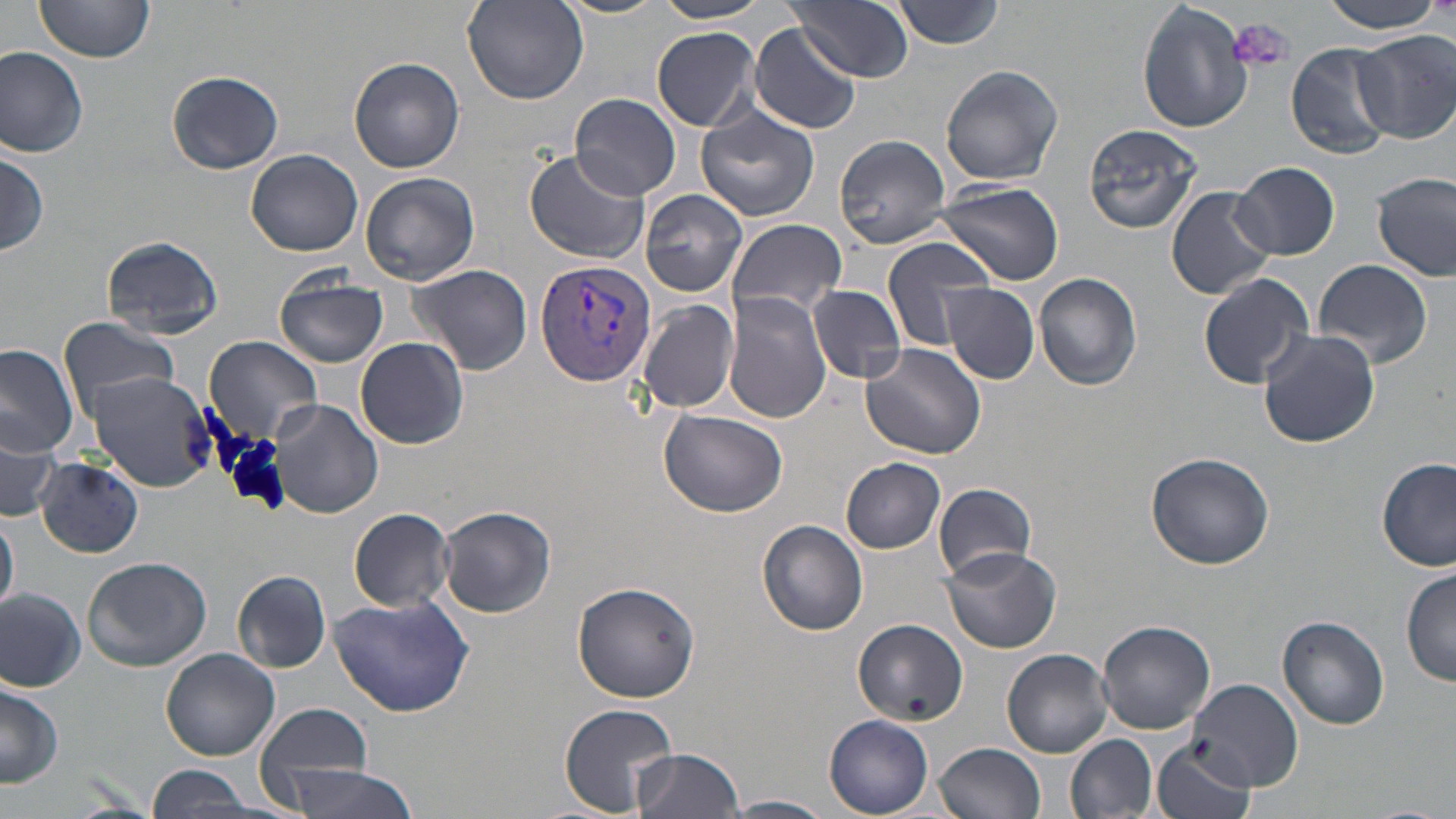 Approximate bounding boxes as (x1,y1)-(x2,y2) corner pairs in pixels. Platelet locations: (1227,18)-(1297,73). Uninfected red blood cell locations: (34,0)-(156,62), (553,0)-(670,18), (653,0)-(776,24), (788,0)-(913,82), (1313,0)-(1450,34), (461,1)-(589,106), (894,1)-(1006,50), (1138,1)-(1253,135), (750,23)-(863,134), (653,26)-(760,130), (1355,32)-(1456,144), (1286,43)-(1393,158), (0,47)-(88,159), (347,57)-(465,173), (940,64)-(1064,186), (164,69)-(284,175), (571,92)-(681,200), (695,106)-(819,223), (1083,124)-(1203,234), (834,134)-(952,249), (1,147)-(50,259), (244,147)-(364,257), (524,149)-(650,264), (1232,163)-(1339,260), (1373,172)-(1455,282), (362,173)-(478,284), (932,183)-(1063,285), (639,187)-(749,296), (1166,187)-(1277,300), (727,218)-(848,321), (102,235)-(224,339), (882,236)-(994,352), (1316,259)-(1434,367), (406,263)-(534,378), (1197,270)-(1317,389), (1034,273)-(1143,392), (274,275)-(389,368), (942,284)-(1040,384), (809,285)-(906,383), (724,293)-(834,422), (636,299)-(739,414), (57,317)-(181,417), (1257,328)-(1382,448), (205,335)-(324,440), (357,337)-(469,450), (858,341)-(987,459), (0,342)-(80,458), (88,372)-(218,492), (270,398)-(384,518), (657,408)-(788,517), (0,415)-(63,522), (1144,451)-(1274,569), (34,458)-(143,558), (841,458)-(946,553), (1376,458)-(1454,571), (933,482)-(1038,582), (438,505)-(556,618), (347,507)-(456,612), (1,513)-(19,615), (756,520)-(867,636), (941,545)-(1059,654), (83,556)-(213,672), (1402,567)-(1456,687), (232,570)-(332,673), (573,580)-(701,701), (0,587)-(86,692), (328,593)-(475,718), (1278,615)-(1391,729), (853,619)-(968,727), (1097,619)-(1215,732), (160,648)-(281,761), (1001,648)-(1112,758), (1188,678)-(1303,792), (1,680)-(65,790), (254,702)-(377,803), (559,703)-(680,815), (825,714)-(934,816), (1066,734)-(1155,818), (1152,736)-(1259,819), (934,742)-(1045,819), (632,747)-(746,819), (284,762)-(424,819), (142,766)-(261,819), (723,795)-(835,818). Plasmodium vivax-infected red blood cell locations: (534,259)-(656,388). Slide-level diagnosis: Plasmodium vivax. Thin blood smear. May-Grünwald-Giemsa stain. Captured at 1000x magnification. Image is 1456×819 pixels. One field of a larger specimen. Optical microscopy.